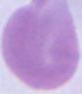

{
  "modality": "photomicrograph",
  "identification": "erythrocyte",
  "magnification": "1000x"
}